Classify this cell by malaria status.
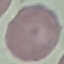
It is uninfected.

Summary:
  - Capture: smartphone camera at the microscope eyepiece
  - Stain: Giemsa
  - Preparation: thin blood smear
  - Image type: automatically extracted cell patch, resized to 64 × 64 pixels